Locate every uninfected red blood cell.
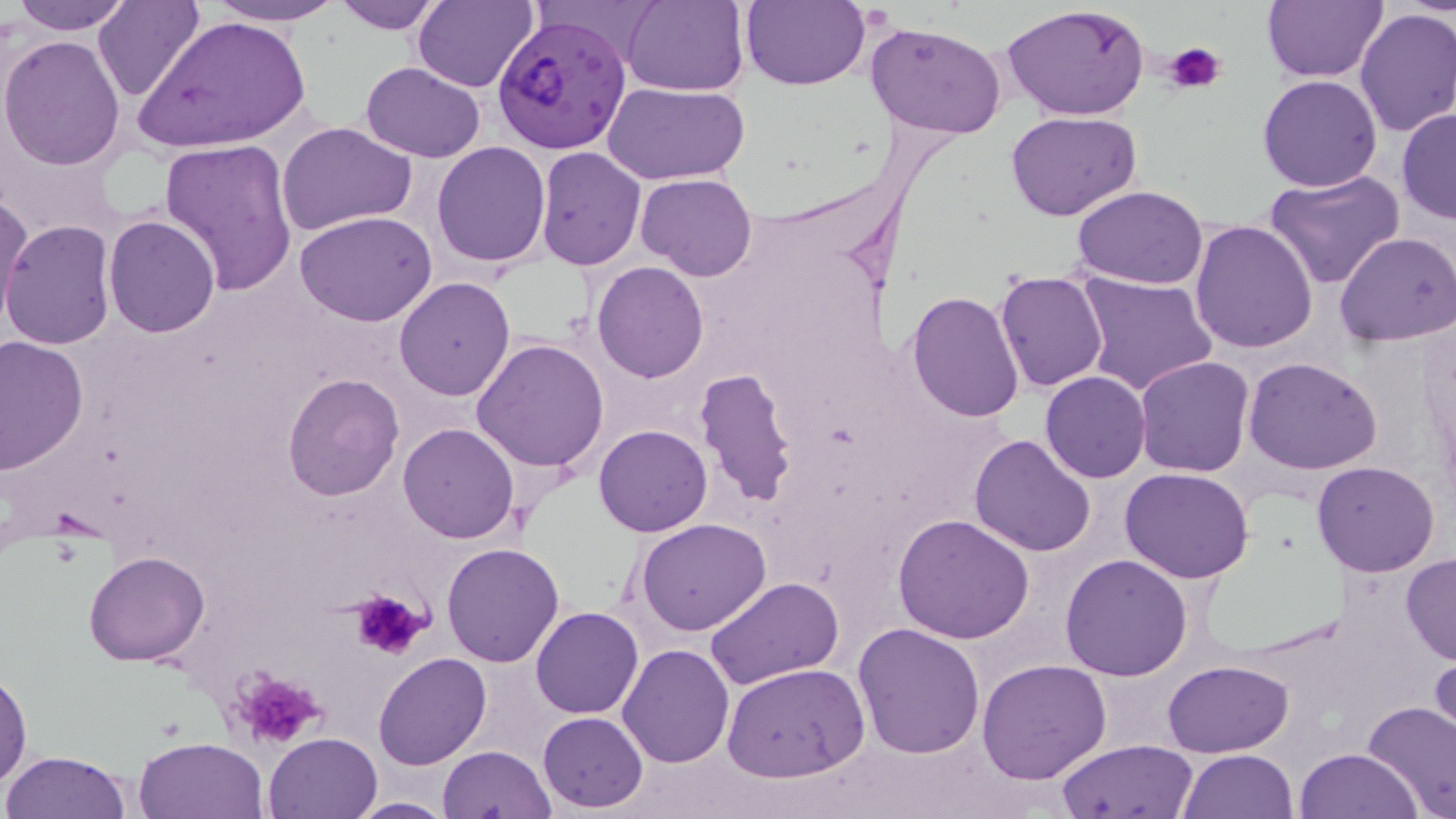

Approximate bounding boxes as [x1, y1, x2, y2] in pixels.
Uninfected red blood cells: [94, 0, 205, 104], [204, 0, 350, 26], [331, 0, 446, 34], [413, 0, 538, 92], [622, 0, 749, 95], [743, 0, 870, 90], [1261, 0, 1385, 82], [11, 1, 131, 35], [1003, 2, 1152, 121], [1353, 8, 1456, 138], [135, 14, 311, 154], [865, 20, 1008, 137], [0, 36, 128, 173], [1280, 44, 1439, 178], [360, 61, 488, 162], [1258, 73, 1383, 191], [606, 82, 750, 184], [1396, 107, 1456, 223], [1008, 111, 1141, 221], [277, 121, 417, 238], [159, 136, 298, 295], [431, 141, 552, 268], [535, 146, 646, 269], [1262, 170, 1408, 292], [636, 173, 757, 281], [1072, 186, 1207, 289], [1, 189, 33, 329], [296, 210, 439, 326], [103, 214, 219, 337], [1189, 219, 1319, 355], [1, 220, 119, 351], [1334, 232, 1456, 346], [592, 262, 709, 382], [995, 271, 1108, 392], [1075, 272, 1216, 397], [395, 276, 516, 400], [905, 291, 1026, 422], [1, 335, 87, 473], [471, 338, 609, 473], [1135, 356, 1253, 477], [1244, 356, 1385, 474], [695, 368, 798, 509], [1040, 370, 1150, 482], [281, 373, 403, 501], [989, 391, 1135, 535], [398, 423, 520, 543], [592, 424, 712, 537], [969, 434, 1096, 556], [1311, 460, 1440, 577], [1121, 467, 1255, 583], [894, 514, 1033, 645], [636, 519, 772, 636], [442, 542, 566, 666], [83, 551, 210, 666], [1060, 554, 1193, 680], [1400, 554, 1456, 666], [704, 577, 844, 691], [531, 606, 644, 718], [854, 623, 986, 759], [617, 643, 736, 767], [1430, 650, 1456, 750], [372, 652, 491, 770], [977, 659, 1112, 783], [1163, 659, 1292, 758], [720, 662, 869, 783], [0, 665, 33, 788], [1361, 702, 1456, 817], [538, 711, 648, 811], [263, 732, 383, 819], [134, 735, 267, 819], [1054, 738, 1200, 818], [437, 745, 557, 818], [1295, 747, 1423, 819], [3, 750, 130, 818], [1176, 750, 1297, 818], [349, 795, 456, 816].

Plasmodium falciparum-infected red blood cell locations: [495, 14, 631, 155]. Platelet locations: [1164, 43, 1227, 94], [350, 590, 430, 660], [229, 667, 329, 748]. Slide-level diagnosis: Plasmodium falciparum. Captured at 1000x magnification. Light microscopy. One field of a larger specimen. May-Grünwald-Giemsa stain. Image is 1456×819 pixels. Thin blood smear.